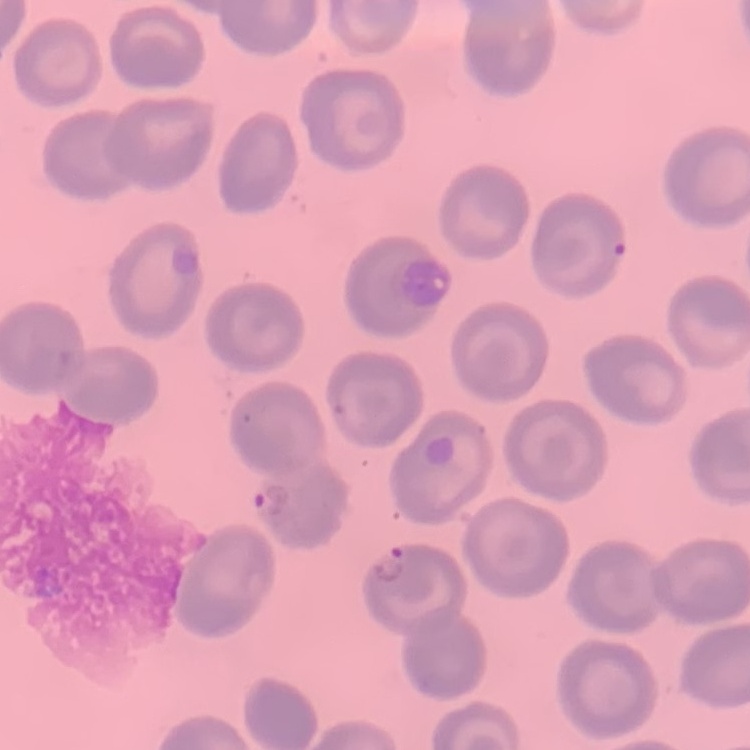

Summary:
  - Erythrocyte morphology: no rouleaux formation
  - Stain: Field's or Giemsa
  - Preparation: thin blood smear
  - Image type: square crop of a larger photomicrograph